Look for Plasmodium parasites.
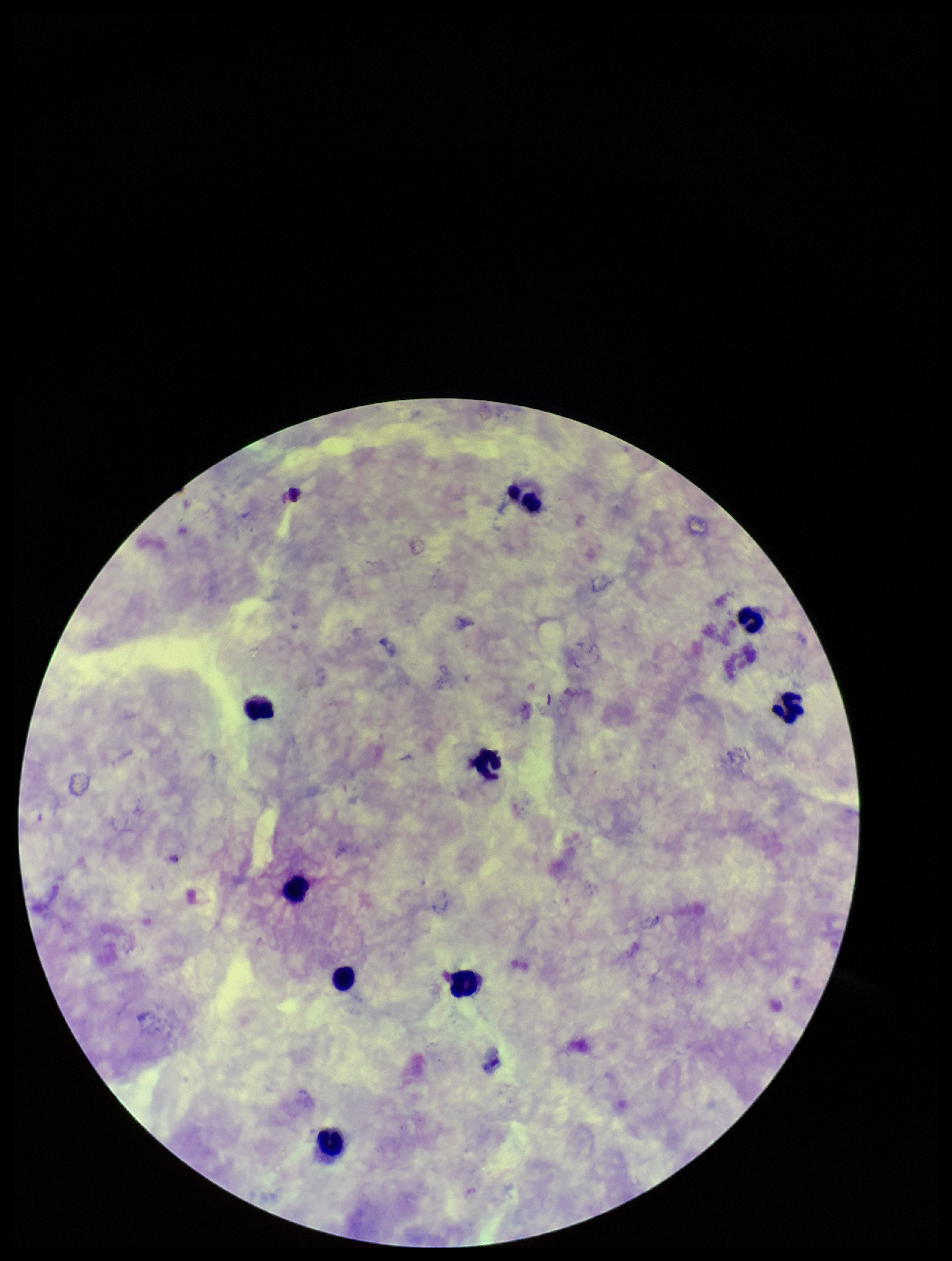
None seen.

Summary:
  - Parasite count: 0
  - Patient malaria status: negative
  - Leukocyte count: 9
  - Preparation: thick smear
  - Capture: smartphone photograph through the microscope eyepiece
  - Field of view: one from this slide
  - Image size: 952×1261 pixels
  - Stain: Giemsa